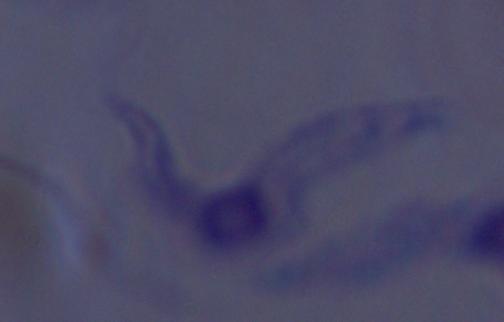
{
  "magnification": "1000x",
  "modality": "photomicrograph",
  "identification": "trypanosome"
}